Report the malaria status of this cell.
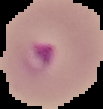
Parasitized.

Summary:
  - Image size: 103×109 pixels
  - Preparation: thin blood film
  - Image type: segmented cell region on a black background